Locate every Plasmodium ovale-infected red blood cell.
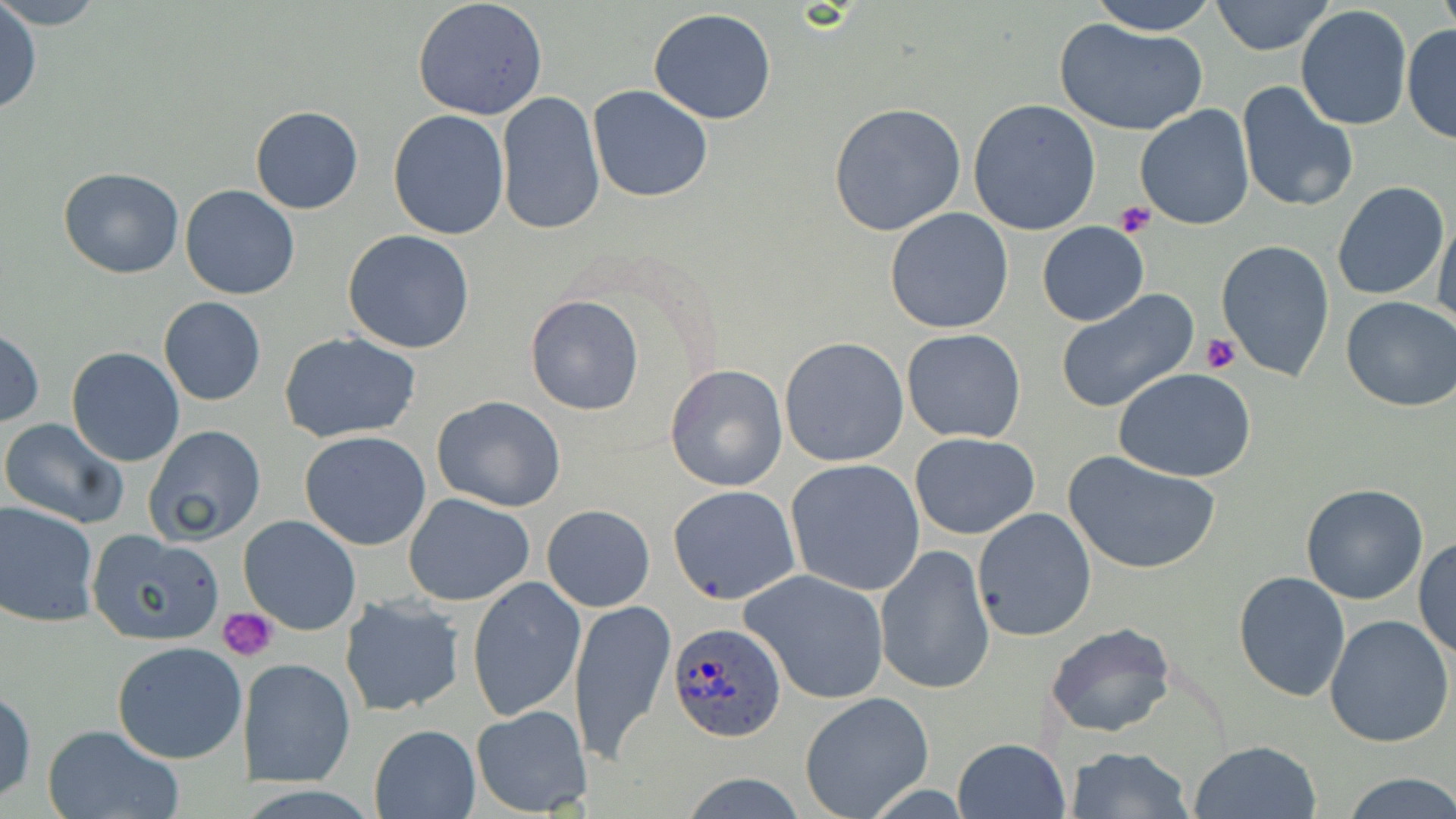
Approximate bounding boxes as (x1, y1, x2, y2) in pixels.
Plasmodium ovale-infected red blood cells: (667, 620, 788, 744).

slide_level_diagnosis: Plasmodium ovale
field_of_view: single
stain: May-Grünwald-Giemsa
magnification: 1000x
image_size: 1456×819 pixels
uninfected_red_blood_cell_locations: 'approximate bounding boxes as (x1, y1, x2, y2) in pixels: (0, 0, 107, 29), (412, 0, 548, 120), (1087, 0, 1220, 34), (1438, 0, 1455, 35), (1211, 1, 1334, 55), (0, 3, 41, 118), (1295, 6, 1413, 131), (648, 8, 777, 125), (1053, 17, 1209, 136), (1402, 22, 1456, 145), (1236, 82, 1359, 214), (586, 85, 713, 203), (495, 92, 605, 237), (967, 100, 1101, 235), (828, 102, 966, 236), (249, 105, 364, 214), (1135, 105, 1254, 230), (387, 110, 510, 241), (58, 167, 184, 278), (1332, 182, 1449, 300), (180, 186, 300, 299), (884, 207, 1015, 334), (1433, 210, 1456, 331), (1037, 222, 1148, 326), (342, 229, 476, 353), (1215, 240, 1336, 382), (1057, 289, 1198, 415), (525, 295, 645, 415), (1341, 295, 1456, 413), (158, 297, 268, 406), (900, 329, 1027, 444), (0, 330, 45, 427), (280, 332, 421, 441), (780, 337, 908, 466), (66, 348, 184, 466), (665, 365, 787, 491), (1113, 366, 1257, 482), (431, 395, 568, 512), (1, 418, 129, 528), (144, 424, 268, 546), (300, 431, 432, 550), (909, 432, 1040, 540), (1063, 450, 1223, 575), (786, 458, 924, 597), (1301, 483, 1429, 605), (667, 485, 799, 604), (402, 493, 535, 606), (0, 500, 99, 627), (543, 504, 655, 612), (972, 507, 1097, 641), (238, 515, 362, 636), (88, 530, 225, 645), (1415, 537, 1455, 663), (877, 545, 996, 696), (740, 568, 891, 705), (1232, 570, 1352, 702), (468, 577, 585, 720), (337, 595, 466, 716), (568, 597, 676, 765), (1325, 613, 1455, 747), (1045, 621, 1176, 740), (110, 641, 247, 765), (241, 658, 354, 787), (1, 687, 36, 804), (798, 693, 932, 818), (471, 705, 593, 815), (42, 725, 186, 819), (370, 725, 479, 817), (953, 738, 1069, 818), (1190, 740, 1321, 819), (1064, 747, 1194, 818), (677, 773, 812, 818), (1340, 774, 1456, 818)'
preparation: thin blood smear
platelet_locations: 'approximate bounding boxes as (x1, y1, x2, y2) in pixels: (1113, 201, 1155, 239), (1201, 334, 1240, 374), (219, 605, 278, 661)'
modality: optical microscopy